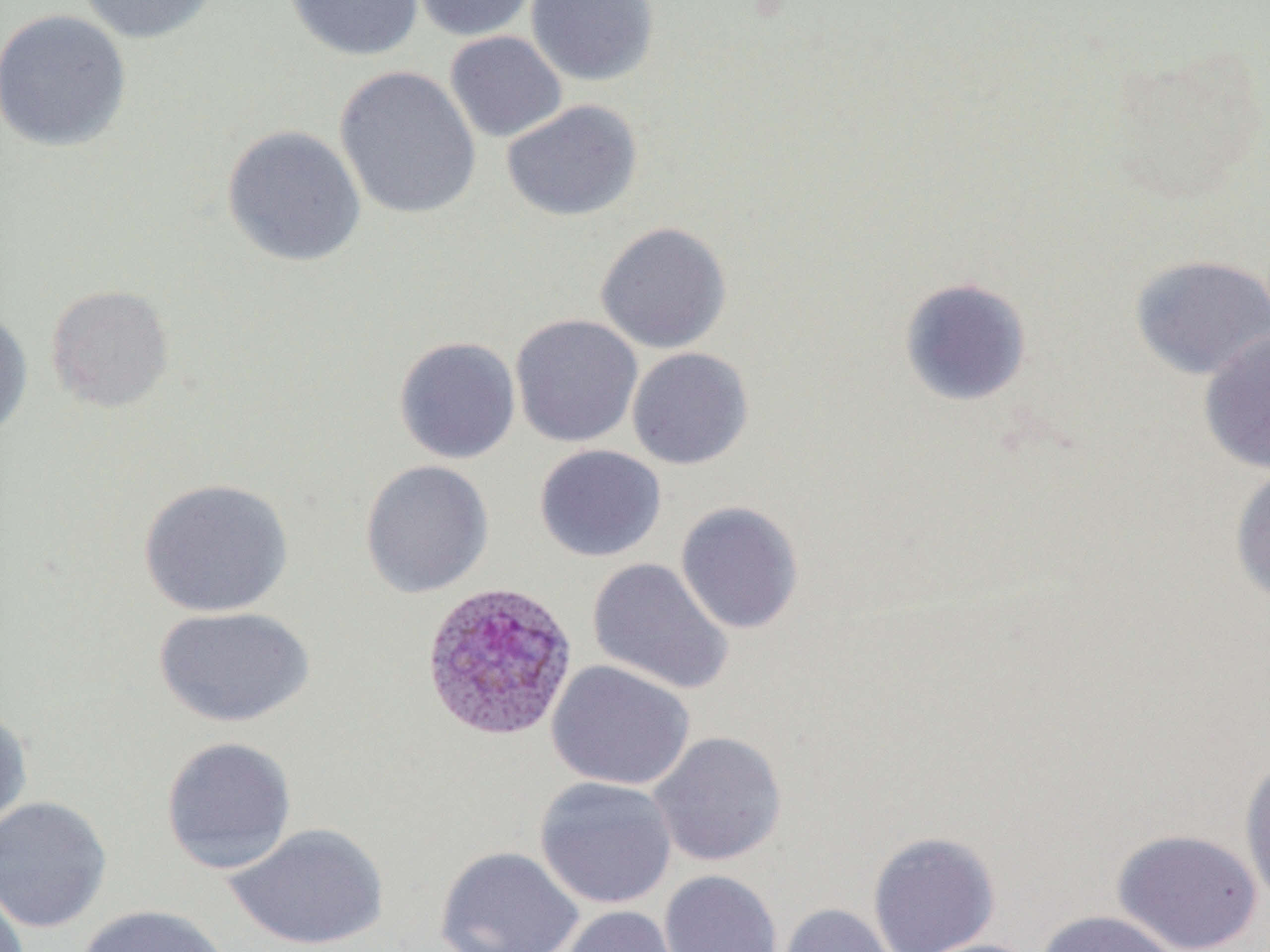
Summary:
  - Coordinate format: approximate bounding boxes as [x1, y1, x2, y2] in pixels
  - Plasmodium ovale-infected red blood cell locations: [420, 581, 579, 743]
  - Uninfected red blood cell locations: [75, 0, 221, 44], [284, 0, 424, 61], [410, 0, 539, 41], [526, 0, 659, 86], [0, 9, 134, 153], [444, 31, 568, 143], [334, 64, 482, 221], [501, 99, 643, 222], [222, 124, 366, 267], [594, 221, 732, 354], [1128, 253, 1270, 381], [898, 277, 1033, 407], [45, 284, 175, 412], [0, 308, 33, 441], [510, 314, 643, 448], [1198, 329, 1270, 474], [392, 336, 521, 464], [626, 347, 754, 470], [534, 444, 666, 563], [359, 459, 494, 599], [1229, 462, 1270, 608], [138, 477, 294, 618], [675, 501, 804, 635], [587, 558, 734, 695], [154, 606, 315, 728], [546, 660, 695, 791], [0, 705, 33, 835], [648, 730, 788, 867], [160, 736, 298, 875], [1238, 754, 1270, 909], [534, 776, 678, 910], [0, 795, 112, 933], [225, 821, 389, 951], [1112, 828, 1262, 952], [867, 831, 1001, 952], [434, 845, 584, 952], [659, 870, 783, 952], [0, 883, 30, 952], [777, 903, 899, 952], [76, 904, 230, 952], [558, 905, 685, 952], [1035, 909, 1182, 952], [907, 938, 1045, 952]
  - Slide-level diagnosis: Plasmodium ovale
  - Field of view: one of a larger specimen
  - Preparation: thin blood smear
  - Stain: May-Grünwald-Giemsa
  - Modality: light microscopy
  - Image size: 1270×952 pixels
  - Magnification: 1000x